State which cell type is depicted.
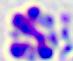
This is a leukocyte.

{
  "modality": "micrograph",
  "magnification": "400x"
}